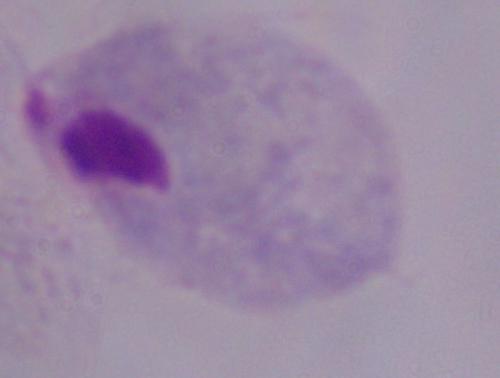

modality = micrograph
identification = trichomonad
magnification = 1000x